Outline every Plasmodium parasite, every leukocyte, and every artifact (stain precipitate or debris).
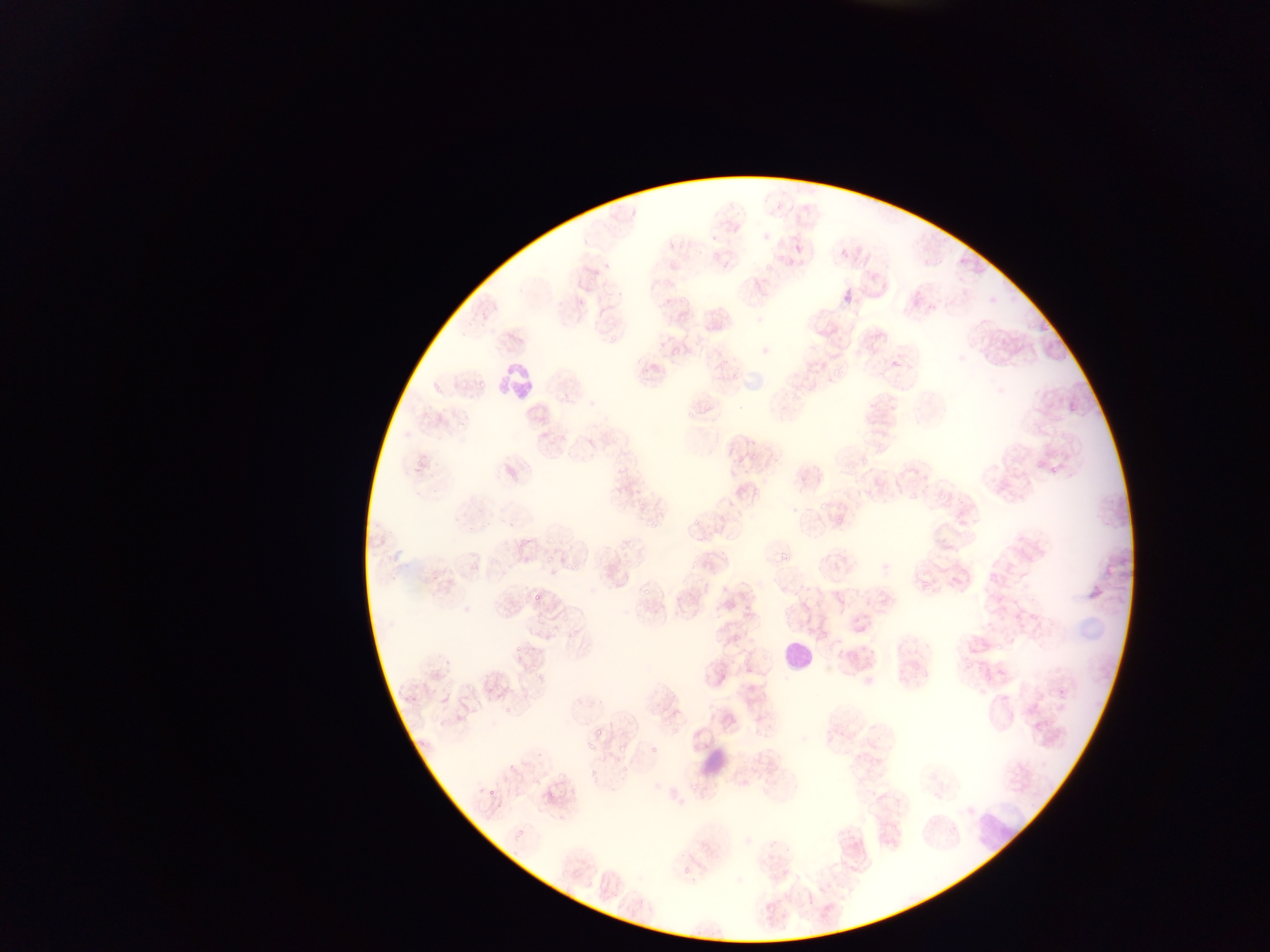
Approximate bounding boxes as (left, top, right, bottom) in pixels.
Plasmodium parasites: (775, 203, 787, 211), (711, 235, 720, 244), (666, 240, 675, 250), (678, 243, 687, 248), (776, 253, 782, 261), (958, 257, 967, 265), (933, 258, 946, 266), (757, 264, 774, 273), (913, 289, 930, 303), (677, 294, 687, 302), (675, 314, 688, 326), (869, 330, 889, 341), (608, 332, 617, 341), (671, 344, 682, 353), (717, 359, 724, 367), (1023, 359, 1031, 365), (890, 360, 901, 371), (650, 363, 661, 373), (829, 372, 840, 382), (730, 373, 738, 378), (432, 378, 448, 392), (477, 379, 489, 390), (1069, 402, 1077, 412), (438, 406, 449, 415), (686, 408, 695, 419), (457, 414, 471, 428), (874, 444, 885, 452), (858, 446, 876, 462), (749, 454, 763, 465), (506, 466, 518, 479), (742, 470, 750, 474), (622, 474, 635, 486), (873, 483, 884, 493), (623, 485, 632, 491), (752, 488, 763, 496), (909, 492, 922, 505), (937, 492, 948, 503), (633, 497, 653, 512), (817, 505, 833, 513), (490, 509, 499, 517), (707, 509, 716, 521), (718, 510, 737, 525), (649, 517, 663, 532), (834, 517, 844, 525), (690, 519, 700, 528), (466, 522, 476, 534), (843, 545, 857, 563), (468, 547, 479, 560), (618, 553, 630, 564), (776, 554, 790, 562), (543, 555, 556, 565), (833, 556, 846, 567), (820, 558, 829, 567), (563, 559, 573, 574), (691, 561, 698, 572), (470, 562, 477, 570), (677, 577, 689, 585), (921, 582, 927, 591), (531, 586, 545, 601), (550, 587, 562, 602), (638, 594, 650, 603), (725, 600, 735, 610), (684, 602, 698, 618), (503, 606, 513, 622), (744, 607, 754, 618), (532, 609, 543, 626), (1029, 611, 1041, 623), (561, 614, 569, 623), (731, 634, 740, 642), (1034, 634, 1042, 640), (995, 639, 1010, 653), (512, 641, 527, 652), (442, 645, 461, 668), (718, 657, 727, 665), (967, 660, 978, 674), (538, 662, 547, 684), (720, 670, 731, 678), (395, 674, 407, 695), (441, 681, 453, 690), (665, 685, 675, 695), (404, 688, 423, 710), (485, 689, 499, 703), (1057, 692, 1067, 702), (469, 696, 485, 714), (503, 699, 520, 720), (574, 703, 585, 716), (643, 707, 655, 716), (656, 709, 666, 719), (729, 709, 735, 724), (1006, 709, 1016, 717), (839, 717, 847, 726), (594, 727, 604, 736), (753, 730, 764, 739), (583, 736, 597, 753), (612, 742, 632, 755), (649, 748, 661, 755), (842, 750, 849, 758), (618, 762, 629, 779), (532, 772, 543, 785), (589, 774, 599, 781), (688, 780, 700, 798), (487, 781, 503, 798), (569, 788, 579, 796), (546, 795, 556, 808), (496, 798, 508, 812), (835, 825, 848, 836), (514, 831, 527, 843), (680, 863, 695, 882), (766, 923, 778, 931) | approximate (x, y) pixel centers of objects too small to bound: (981, 349), (996, 363), (419, 464), (1053, 470), (454, 517), (808, 528), (551, 574), (686, 599), (525, 666), (535, 674), (677, 709).
Leukocytes: (499, 358, 533, 396), (780, 639, 814, 671), (702, 750, 736, 781), (961, 803, 1034, 852).

Summary:
  - Field of view: single
  - Preparation: thin blood film
  - Country: Ghana
  - Image size: 1270×952 pixels
  - Capture: mobile-phone photograph through a microscope